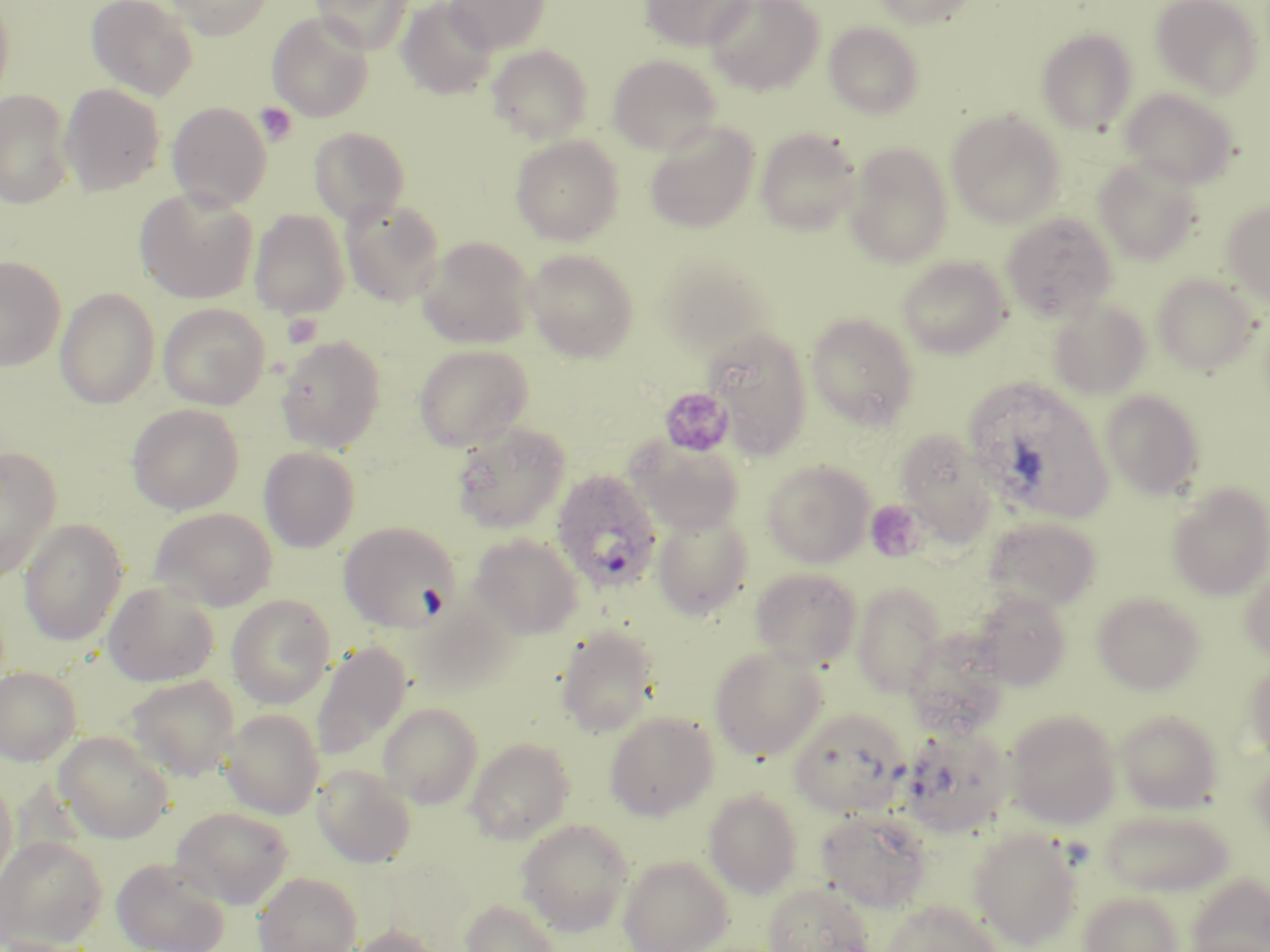
Summary:
  - Coordinate format: approximate bounding boxes as (x1,y1)-(x2,y2) corner pairs in pixels
  - Plasmodium ovale-infected red blood cell locations: (552,469)-(663,591)
  - Platelet locations: (254,103)-(297,145), (282,313)-(323,348), (659,388)-(735,457), (866,500)-(925,562)
  - Uninfected red blood cell locations: (0,0)-(15,108), (86,0)-(199,100), (166,0)-(274,39), (310,0)-(415,52), (396,0)-(498,99), (445,0)-(550,54), (640,0)-(753,52), (705,0)-(824,95), (873,0)-(977,29), (1150,0)-(1264,99), (266,12)-(375,122), (824,22)-(924,119), (1036,28)-(1138,135), (486,44)-(593,144), (607,54)-(722,155), (59,84)-(166,196), (1120,87)-(1240,188), (0,89)-(75,209), (167,101)-(272,211), (946,109)-(1065,228), (645,122)-(759,233), (308,126)-(410,225), (755,126)-(862,236), (510,135)-(624,246), (844,143)-(953,268), (1094,157)-(1202,265), (135,189)-(259,304), (341,199)-(445,307), (1222,201)-(1270,306), (249,210)-(350,318), (1001,212)-(1118,321), (417,236)-(535,349), (525,249)-(639,362), (657,251)-(774,355), (0,256)-(66,371), (896,256)-(1011,359), (1152,273)-(1259,375), (55,287)-(160,409), (1048,298)-(1152,400), (158,303)-(270,409), (807,312)-(919,429), (703,326)-(813,456), (275,335)-(386,453), (413,344)-(533,452), (973,389)-(1118,519), (1100,389)-(1206,499), (127,404)-(244,515), (452,422)-(570,533), (894,430)-(997,543), (631,437)-(744,535), (0,445)-(62,580), (259,446)-(361,552), (762,460)-(875,567), (1165,482)-(1270,601), (149,507)-(278,612), (652,511)-(753,619), (983,516)-(1102,613), (19,518)-(128,646), (338,521)-(461,631), (469,533)-(584,639), (750,567)-(862,669), (1239,569)-(1270,665), (102,581)-(220,687), (852,583)-(946,696), (971,590)-(1071,691), (1093,591)-(1205,695), (227,595)-(335,709), (556,625)-(661,736), (905,631)-(1010,736), (311,641)-(412,761), (709,646)-(827,760), (1244,660)-(1270,766), (0,666)-(82,766), (126,676)-(239,782), (378,703)-(483,808), (221,709)-(323,819), (788,709)-(910,817), (1004,710)-(1121,829), (1116,710)-(1223,814), (605,711)-(719,820), (896,725)-(1013,837), (53,732)-(173,843), (466,737)-(574,843), (312,763)-(417,868), (0,771)-(17,893), (703,789)-(803,898), (171,807)-(294,910), (816,808)-(933,912), (1100,808)-(1234,896), (516,819)-(633,935), (969,826)-(1084,950), (0,836)-(107,950), (618,854)-(733,952), (111,856)-(230,952), (253,872)-(362,952), (1185,875)-(1270,952), (763,884)-(875,952), (1079,892)-(1184,952), (460,899)-(562,952), (879,901)-(1003,952), (347,923)-(446,952), (1,936)-(102,952)
  - Slide-level diagnosis: Plasmodium ovale
  - Magnification: 1000x
  - Field of view: single
  - Preparation: thin blood smear
  - Modality: optical microscopy
  - Stain: May-Grünwald-Giemsa
  - Image size: 1270×952 pixels